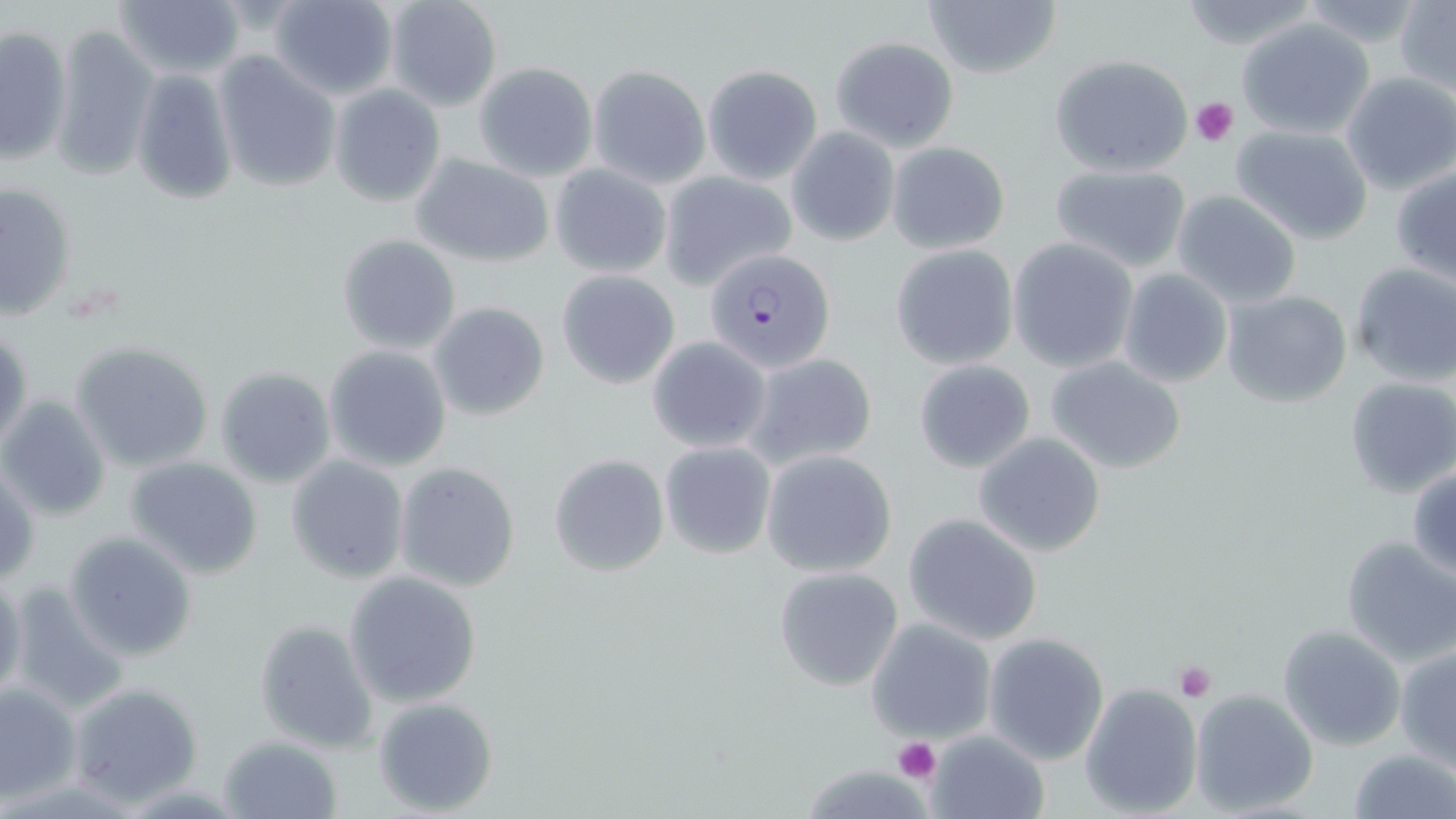 Approximate bounding boxes as [x1, y1, x2, y2] in pixels. Plasmodium falciparum-infected red blood cell locations: [706, 247, 838, 372]. Platelet locations: [1189, 97, 1240, 147], [1173, 660, 1217, 702], [892, 738, 940, 784]. Uninfected red blood cell locations: [112, 0, 248, 79], [268, 0, 399, 100], [383, 0, 504, 111], [923, 0, 1061, 80], [1175, 0, 1323, 51], [1294, 0, 1431, 46], [1396, 0, 1456, 94], [1234, 14, 1378, 139], [45, 21, 157, 180], [0, 26, 71, 163], [830, 36, 958, 151], [213, 51, 341, 193], [1048, 53, 1195, 176], [473, 62, 598, 180], [703, 63, 822, 183], [587, 64, 711, 188], [129, 69, 237, 205], [1341, 72, 1456, 194], [330, 84, 447, 208], [1230, 123, 1375, 245], [787, 128, 900, 246], [886, 140, 1011, 254], [411, 155, 555, 266], [548, 163, 673, 278], [1390, 163, 1456, 284], [1047, 164, 1191, 273], [657, 171, 798, 288], [2, 182, 78, 320], [1172, 190, 1303, 308], [336, 233, 461, 355], [1008, 237, 1138, 371], [890, 243, 1018, 369], [1347, 263, 1456, 387], [1117, 268, 1232, 388], [556, 269, 681, 389], [1221, 289, 1354, 408], [428, 302, 551, 422], [1, 324, 31, 456], [647, 336, 773, 451], [68, 341, 216, 470], [322, 345, 452, 471], [742, 352, 880, 471], [1045, 355, 1188, 473], [913, 361, 1037, 474], [214, 366, 337, 488], [1343, 376, 1456, 498], [1, 395, 112, 519], [973, 431, 1107, 556], [659, 441, 777, 557], [760, 450, 898, 577], [286, 454, 409, 583], [547, 454, 670, 576], [126, 456, 265, 579], [394, 462, 522, 592], [0, 463, 41, 589], [1407, 467, 1456, 578], [903, 515, 1042, 645], [65, 531, 197, 661], [1339, 535, 1456, 667], [775, 566, 904, 690], [343, 570, 483, 708], [0, 572, 26, 706], [3, 584, 127, 715], [252, 619, 378, 753], [866, 620, 996, 743], [1277, 625, 1406, 751], [982, 632, 1109, 764], [1394, 645, 1456, 768], [67, 681, 203, 805], [1079, 682, 1203, 817], [0, 684, 81, 804], [1189, 688, 1319, 816], [372, 696, 498, 816], [926, 730, 1051, 819], [219, 734, 342, 818], [1347, 747, 1455, 819]. Slide-level diagnosis: Plasmodium falciparum. Thin blood smear. 1000x magnification. Image is 1456×819 pixels. Light microscopy. May-Grünwald-Giemsa stain. One field of a larger specimen.